Classify this cell by malaria status.
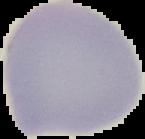
It is uninfected.

{
  "preparation": "thin blood smear",
  "image_type": "segmented cell region on a black background",
  "image_size": "145×139 pixels"
}